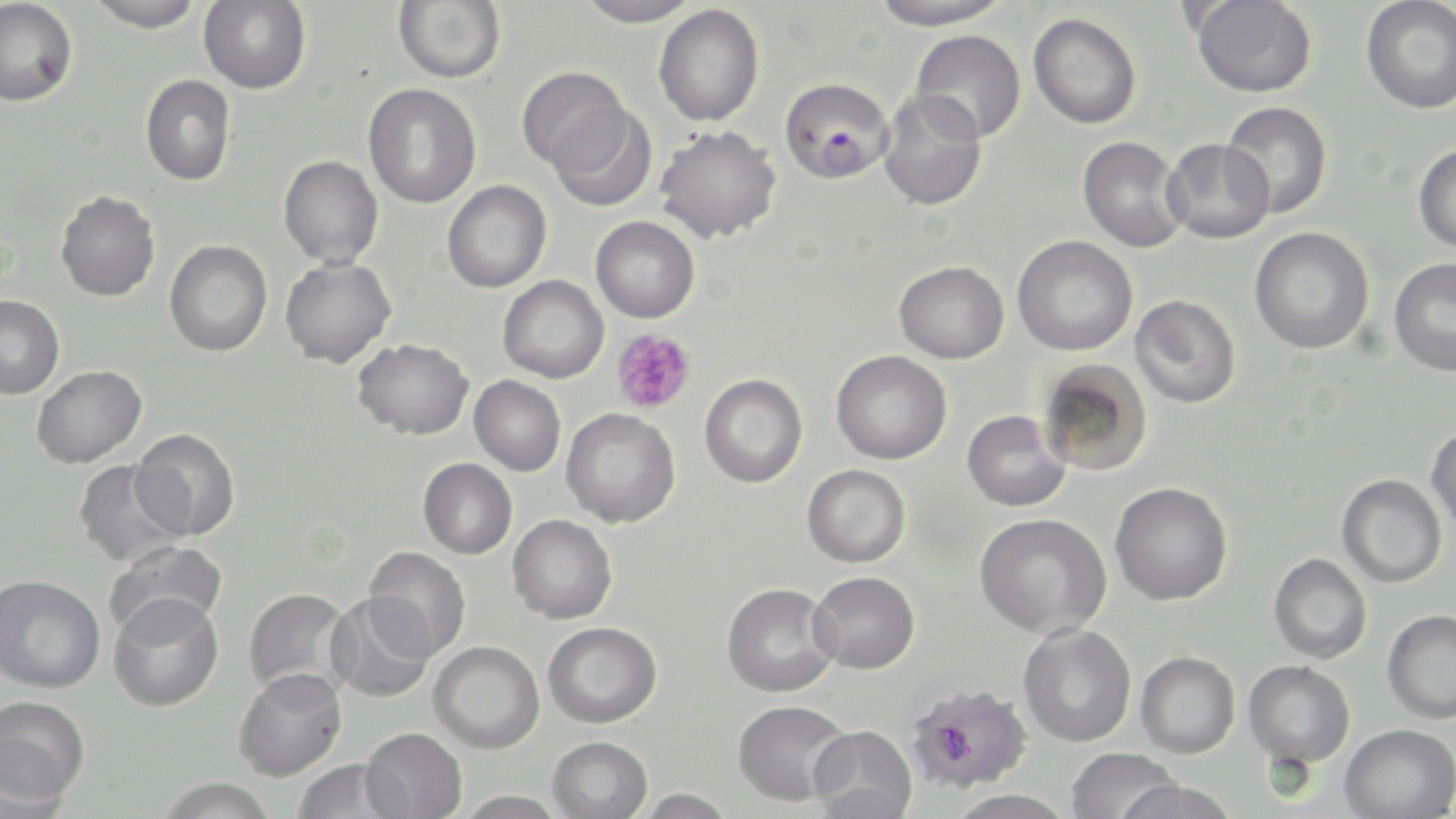
slide_level_diagnosis: Plasmodium falciparum
modality: optical microscopy
plasmodium_falciparum_infected_red_blood_cell_locations: 'approximate bounding boxes as named x1/y1/x2/y2 corners in pixels: (x1=779, y1=77, x2=894, y2=184)'
field_of_view: one of a larger specimen
preparation: thin blood film
stain: May-Grünwald-Giemsa
image_size: 1456×819 pixels
magnification: 1000x
uninfected_red_blood_cell_locations: 'approximate bounding boxes as named x1/y1/x2/y2 corners in pixels: (x1=0, y1=0, x2=78, y2=106), (x1=86, y1=0, x2=205, y2=32), (x1=199, y1=0, x2=311, y2=94), (x1=393, y1=0, x2=506, y2=84), (x1=574, y1=0, x2=701, y2=27), (x1=867, y1=0, x2=1014, y2=30), (x1=1191, y1=0, x2=1317, y2=98), (x1=1361, y1=0, x2=1456, y2=114), (x1=653, y1=4, x2=765, y2=127), (x1=1028, y1=12, x2=1142, y2=129), (x1=910, y1=29, x2=1026, y2=143), (x1=517, y1=67, x2=632, y2=173), (x1=140, y1=74, x2=236, y2=186), (x1=363, y1=83, x2=482, y2=208), (x1=877, y1=88, x2=987, y2=212), (x1=1220, y1=101, x2=1333, y2=219), (x1=547, y1=104, x2=656, y2=212), (x1=654, y1=125, x2=782, y2=244), (x1=1077, y1=136, x2=1189, y2=253), (x1=1162, y1=138, x2=1274, y2=245), (x1=1413, y1=143, x2=1456, y2=252), (x1=279, y1=155, x2=384, y2=268), (x1=442, y1=180, x2=551, y2=293), (x1=55, y1=190, x2=161, y2=301), (x1=591, y1=216, x2=700, y2=323), (x1=1249, y1=227, x2=1374, y2=354), (x1=1012, y1=235, x2=1137, y2=356), (x1=165, y1=240, x2=272, y2=356), (x1=280, y1=257, x2=397, y2=368), (x1=1388, y1=258, x2=1456, y2=376), (x1=894, y1=261, x2=1009, y2=363), (x1=497, y1=275, x2=609, y2=383), (x1=0, y1=295, x2=64, y2=398), (x1=1129, y1=295, x2=1241, y2=408), (x1=352, y1=338, x2=473, y2=439), (x1=831, y1=350, x2=952, y2=464), (x1=1039, y1=359, x2=1154, y2=477), (x1=32, y1=365, x2=146, y2=468), (x1=699, y1=374, x2=808, y2=488), (x1=469, y1=375, x2=566, y2=476), (x1=561, y1=408, x2=680, y2=528), (x1=962, y1=409, x2=1070, y2=512), (x1=1426, y1=425, x2=1456, y2=534), (x1=131, y1=428, x2=240, y2=541), (x1=418, y1=458, x2=517, y2=559), (x1=74, y1=460, x2=187, y2=567), (x1=802, y1=464, x2=910, y2=568), (x1=1336, y1=474, x2=1447, y2=588), (x1=1110, y1=481, x2=1232, y2=605), (x1=975, y1=513, x2=1111, y2=638), (x1=508, y1=514, x2=617, y2=623), (x1=105, y1=540, x2=227, y2=639), (x1=363, y1=546, x2=471, y2=659), (x1=1268, y1=553, x2=1372, y2=663), (x1=809, y1=571, x2=919, y2=673), (x1=0, y1=574, x2=105, y2=693), (x1=722, y1=582, x2=840, y2=697), (x1=243, y1=587, x2=356, y2=700), (x1=108, y1=592, x2=224, y2=711), (x1=325, y1=592, x2=436, y2=703), (x1=1382, y1=609, x2=1456, y2=723), (x1=543, y1=621, x2=662, y2=727), (x1=1018, y1=624, x2=1136, y2=746), (x1=429, y1=641, x2=544, y2=753), (x1=1136, y1=651, x2=1240, y2=758), (x1=1244, y1=659, x2=1355, y2=766), (x1=234, y1=667, x2=346, y2=781), (x1=903, y1=681, x2=1033, y2=793), (x1=1, y1=695, x2=91, y2=806), (x1=732, y1=699, x2=854, y2=806), (x1=1340, y1=724, x2=1455, y2=818), (x1=809, y1=726, x2=917, y2=818), (x1=361, y1=727, x2=468, y2=819), (x1=548, y1=736, x2=652, y2=819), (x1=1065, y1=747, x2=1180, y2=819), (x1=292, y1=759, x2=409, y2=819), (x1=157, y1=777, x2=278, y2=819), (x1=1115, y1=780, x2=1240, y2=819), (x1=632, y1=788, x2=737, y2=819), (x1=945, y1=789, x2=1078, y2=818), (x1=454, y1=790, x2=568, y2=818)'
platelet_locations: 'approximate bounding boxes as named x1/y1/x2/y2 corners in pixels: (x1=611, y1=329, x2=696, y2=414)'